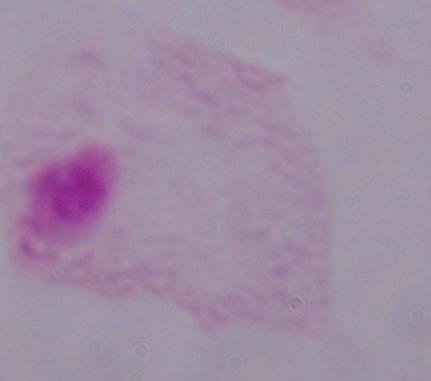
Summary:
  - Identification: trichomonad
  - Modality: photomicrograph
  - Magnification: 1000x